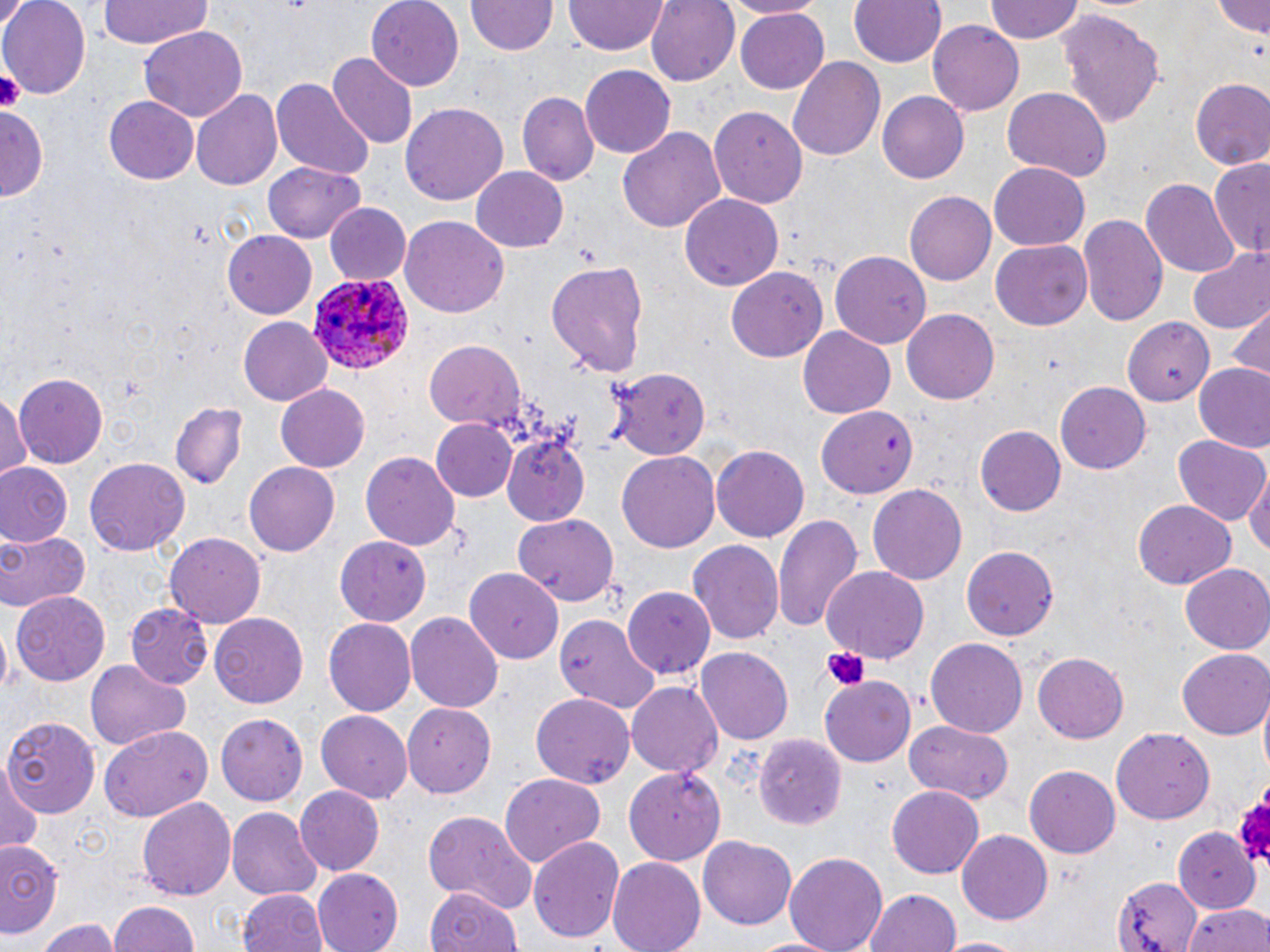
slide_level_diagnosis: Plasmodium ovale
image_size: 1270×952 pixels
preparation: thin blood smear
uninfected_red_blood_cell_locations: 'approximate bounding boxes as [x1, y1, x2, y2] in pixels: [0, 0, 88, 96], [97, 0, 211, 51], [368, 0, 465, 91], [565, 0, 667, 57], [645, 0, 739, 87], [721, 0, 824, 18], [850, 0, 946, 67], [987, 0, 1083, 43], [1212, 0, 1268, 36], [466, 2, 556, 57], [0, 3, 25, 41], [736, 7, 831, 93], [1059, 10, 1167, 128], [927, 21, 1025, 116], [140, 25, 248, 121], [327, 53, 417, 150], [786, 56, 884, 163], [580, 64, 674, 156], [273, 77, 374, 179], [1190, 79, 1270, 172], [1002, 89, 1112, 183], [191, 90, 281, 191], [878, 91, 970, 183], [517, 92, 598, 186], [102, 95, 199, 185], [400, 103, 507, 208], [708, 104, 807, 205], [0, 107, 47, 204], [617, 126, 726, 234], [1208, 159, 1270, 265], [990, 161, 1090, 248], [263, 162, 366, 243], [472, 166, 569, 252], [1142, 176, 1240, 277], [905, 192, 996, 283], [679, 193, 784, 293], [325, 201, 411, 285], [1078, 213, 1166, 326], [400, 217, 508, 319], [223, 228, 319, 318], [991, 241, 1093, 330], [1187, 249, 1270, 334], [830, 251, 931, 350], [545, 259, 650, 378], [726, 267, 828, 362], [1227, 304, 1268, 384], [902, 308, 1002, 404], [1121, 315, 1213, 405], [237, 317, 332, 405], [800, 327, 896, 418], [425, 339, 526, 431], [1192, 364, 1270, 453], [610, 365, 711, 458], [13, 372, 110, 468], [1055, 383, 1151, 474], [276, 384, 371, 473], [1, 391, 31, 478], [168, 403, 246, 488], [817, 405, 917, 497], [430, 418, 517, 503], [976, 425, 1066, 517], [1173, 435, 1269, 526], [503, 436, 588, 525], [711, 447, 810, 542], [616, 450, 721, 555], [360, 452, 461, 551], [86, 458, 189, 556], [244, 461, 340, 556], [0, 463, 72, 548], [1245, 471, 1270, 565], [866, 484, 968, 587], [1133, 500, 1235, 588], [773, 509, 862, 632], [511, 513, 619, 607], [0, 528, 92, 612], [167, 533, 265, 629], [336, 536, 436, 624], [688, 539, 785, 644], [959, 545, 1058, 642], [1181, 565, 1270, 655], [823, 566, 929, 662], [465, 568, 563, 663], [622, 585, 718, 679], [11, 591, 112, 686], [125, 604, 213, 690], [211, 611, 308, 707], [407, 612, 502, 714], [554, 615, 660, 714], [324, 619, 416, 716], [924, 637, 1028, 739], [697, 648, 794, 744], [1179, 649, 1270, 739], [1032, 651, 1129, 743], [84, 659, 194, 751], [820, 676, 915, 767], [627, 680, 723, 779], [531, 692, 633, 788], [402, 702, 495, 799], [316, 710, 413, 803], [217, 713, 308, 806], [4, 716, 101, 816], [902, 718, 1015, 804], [100, 726, 212, 823], [1112, 730, 1214, 823], [754, 734, 844, 831], [1, 760, 42, 855], [623, 766, 725, 866], [1024, 766, 1119, 859], [500, 774, 608, 869], [887, 784, 985, 879], [295, 786, 385, 877], [135, 796, 236, 901], [225, 807, 322, 901], [423, 809, 537, 913], [958, 828, 1054, 924], [1169, 828, 1257, 908], [698, 835, 797, 930], [529, 836, 624, 944], [0, 840, 66, 939], [782, 851, 887, 952], [607, 856, 706, 952], [312, 869, 403, 951], [1114, 875, 1206, 952], [862, 885, 962, 952], [422, 886, 525, 952], [236, 889, 327, 952], [108, 899, 198, 952], [1184, 902, 1270, 952], [37, 919, 119, 952], [751, 934, 839, 952], [939, 936, 1028, 952]'
field_of_view: one of a larger specimen
stain: May-Grünwald-Giemsa
plasmodium_ovale_infected_red_blood_cell_locations: 'approximate bounding boxes as [x1, y1, x2, y2] in pixels: [307, 269, 417, 373]'
modality: light microscopy
platelet_locations: 'approximate bounding boxes as [x1, y1, x2, y2] in pixels: [0, 69, 23, 111], [824, 647, 866, 690], [1229, 792, 1270, 869]'
magnification: 1000x